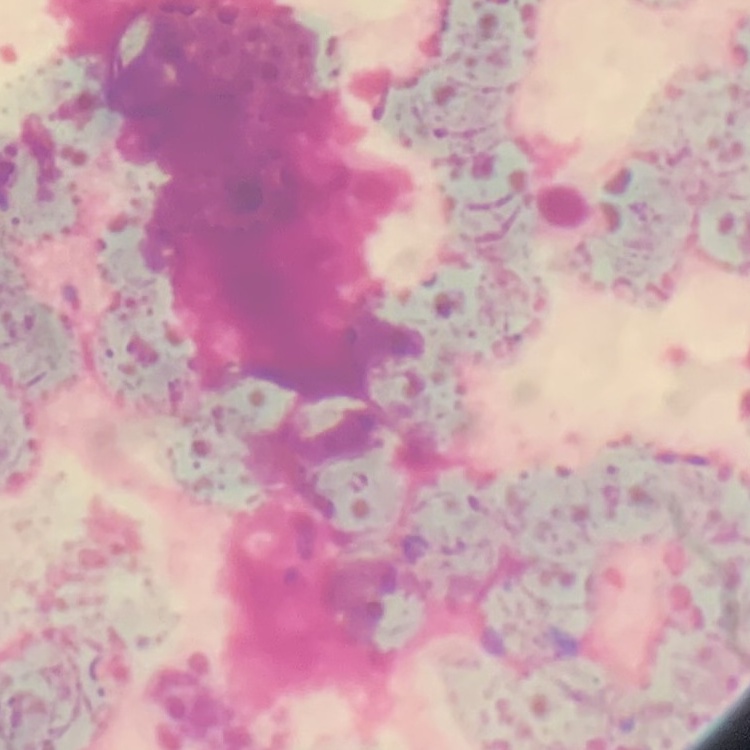

{
  "erythrocyte_morphology": "rouleaux formation",
  "image_type": "one tile cut from a larger photomicrograph",
  "stain": "Field's or Giemsa",
  "preparation": "thin peripheral smear"
}